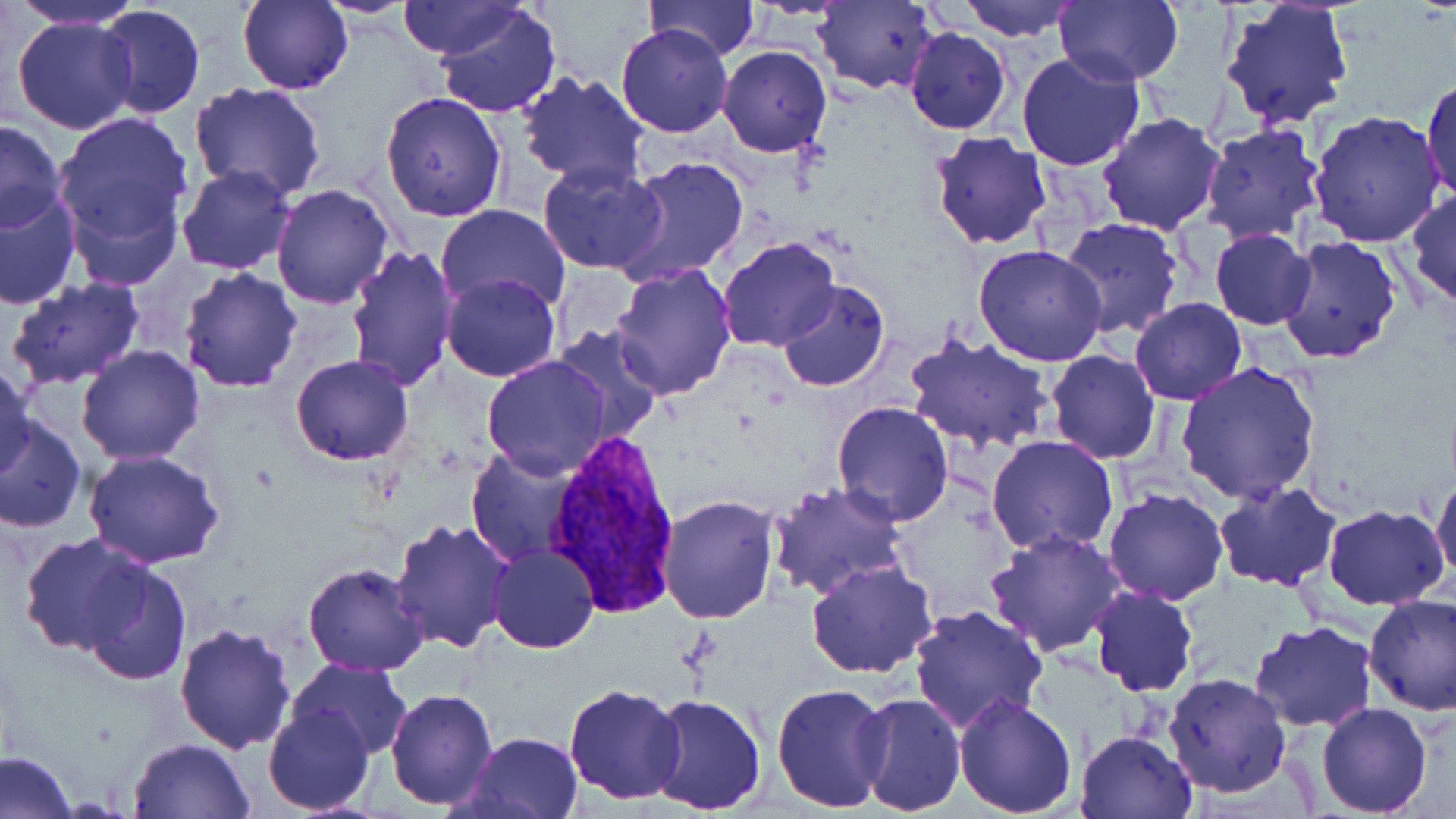
Summary:
  - Coordinate format: approximate bounding boxes as [x1, y1, x2, y2] in pixels
  - Uninfected red blood cell locations: [314, 0, 423, 18], [397, 0, 527, 61], [644, 0, 760, 64], [812, 0, 937, 93], [958, 0, 1079, 42], [1054, 0, 1184, 85], [8, 1, 143, 30], [240, 1, 352, 95], [1219, 1, 1355, 131], [434, 2, 561, 119], [96, 4, 206, 121], [11, 15, 138, 135], [616, 24, 734, 138], [904, 26, 1011, 134], [718, 45, 831, 157], [1016, 50, 1146, 171], [517, 70, 650, 192], [1421, 79, 1455, 203], [190, 83, 329, 202], [381, 93, 507, 223], [49, 108, 195, 274], [1308, 111, 1446, 248], [1096, 113, 1225, 235], [0, 121, 67, 231], [1200, 122, 1326, 244], [930, 131, 1052, 248], [612, 156, 749, 286], [536, 161, 668, 275], [176, 164, 297, 276], [270, 184, 395, 309], [1, 188, 81, 309], [1405, 190, 1456, 308], [438, 203, 571, 313], [1056, 216, 1184, 339], [1207, 228, 1316, 330], [717, 237, 839, 353], [1275, 237, 1401, 364], [345, 243, 460, 392], [974, 244, 1108, 367], [610, 261, 740, 399], [179, 266, 303, 390], [441, 271, 561, 382], [6, 277, 145, 390], [776, 280, 891, 392], [1129, 297, 1247, 405], [549, 324, 665, 443], [905, 334, 1055, 455], [76, 344, 204, 465], [1045, 349, 1160, 463], [291, 354, 412, 465], [480, 356, 612, 479], [0, 362, 36, 478], [1176, 363, 1323, 506], [831, 400, 955, 527], [0, 416, 86, 535], [985, 436, 1119, 556], [466, 446, 585, 565], [82, 451, 225, 569], [1431, 473, 1456, 585], [1213, 480, 1344, 592], [766, 483, 910, 602], [1103, 490, 1228, 606], [658, 495, 780, 624], [1323, 504, 1450, 610], [389, 518, 512, 652], [987, 529, 1124, 657], [19, 533, 151, 656], [488, 544, 598, 653], [805, 560, 937, 680], [81, 562, 192, 686], [304, 562, 429, 677], [1088, 586, 1200, 696], [1363, 593, 1456, 714], [907, 604, 1048, 735], [1249, 621, 1378, 733], [174, 622, 298, 755], [291, 657, 413, 758], [1164, 672, 1292, 797], [771, 682, 890, 811], [563, 683, 688, 803], [385, 688, 498, 809], [852, 691, 967, 816], [647, 692, 767, 816], [951, 692, 1078, 816], [1317, 702, 1433, 817], [264, 707, 374, 814], [1075, 729, 1197, 818], [464, 731, 582, 819], [128, 737, 255, 819], [0, 750, 79, 819]
  - Plasmodium vivax-infected red blood cell locations: [541, 432, 684, 618]
  - Slide-level diagnosis: Plasmodium vivax
  - Preparation: thin blood smear
  - Modality: optical microscopy
  - Magnification: 1000x
  - Stain: May-Grünwald-Giemsa
  - Image size: 1456×819 pixels
  - Field of view: one of a larger specimen